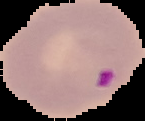 Segmented cell region on a black background. From a thin blood smear. Malaria status: parasitized. Image is 145×121 pixels.